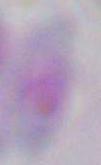

Photomicrograph. 1000x magnification. Toxoplasma gondii is seen.